Assess the morphology of the red blood cells.
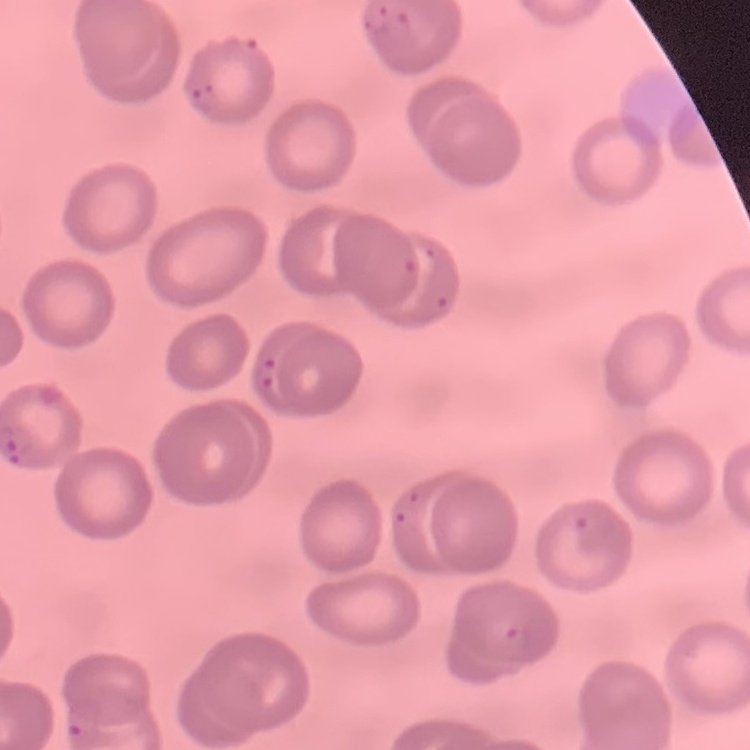

They show no rouleaux formation.

Square crop of a larger photomicrograph. Thin peripheral smear. Field's or Giemsa stain.